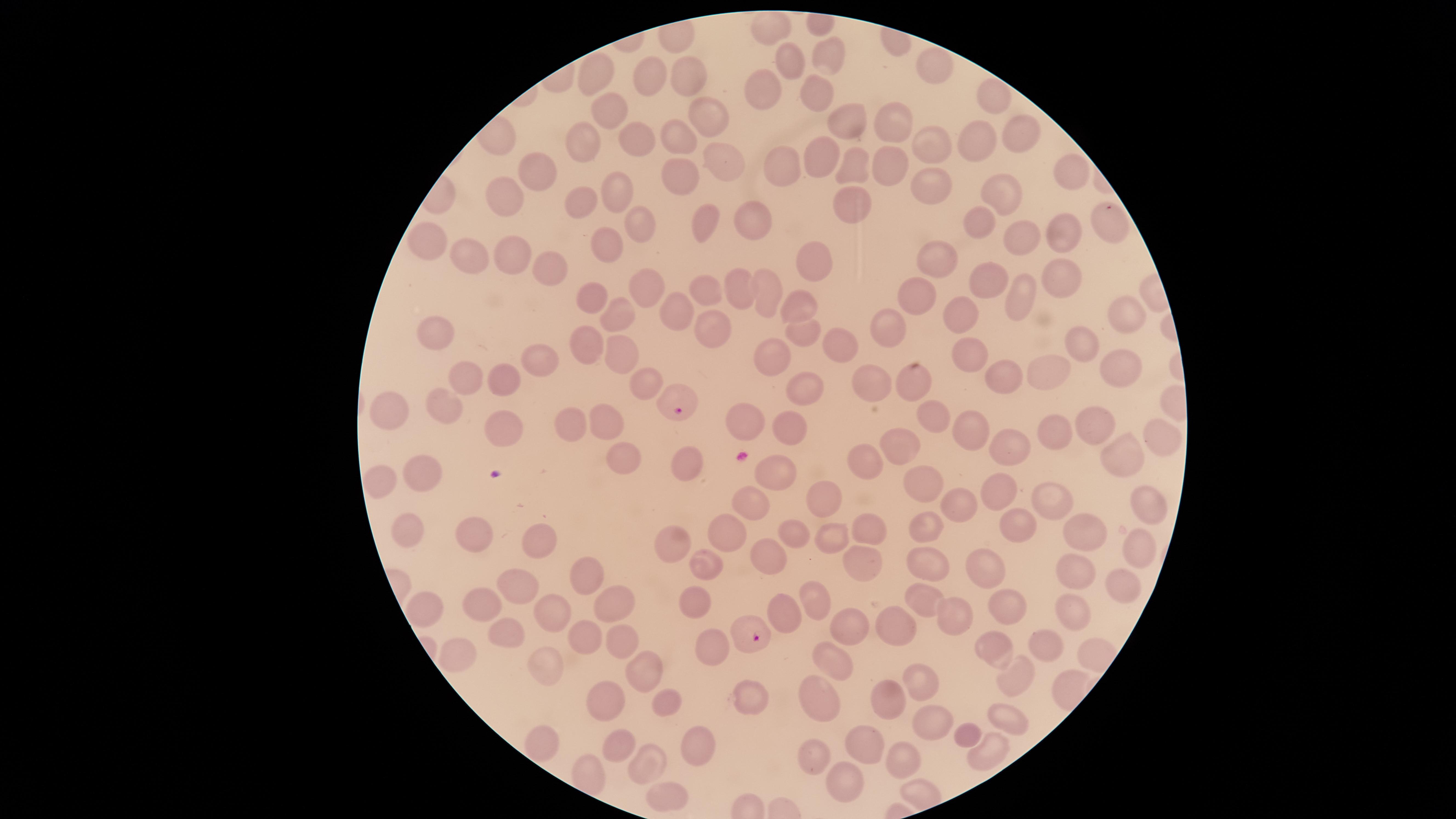
presence = malaria parasites seen
species = Plasmodium falciparum
parasitized RBCs = approximate marker points as [x, y] in pixels: [677, 403], [752, 635]
stain = Giemsa
uninfected RBCs = approximate marker points as [x, y] in pixels: [771, 21], [826, 53], [797, 61], [933, 67], [648, 75], [687, 76], [595, 80], [761, 85], [816, 93], [994, 96], [613, 108], [708, 118], [849, 120], [896, 121], [1023, 134], [638, 135], [975, 140], [588, 141], [680, 142], [931, 149], [812, 156], [782, 162], [884, 162], [722, 164], [850, 164], [1068, 167], [540, 170], [680, 176], [939, 184], [614, 186], [1001, 195], [507, 198], [582, 202], [850, 207], [752, 215], [1106, 218], [636, 224], [703, 224], [976, 226], [1061, 233], [1022, 237], [430, 243], [611, 244], [473, 251], [515, 256], [937, 256], [807, 260], [553, 270], [1059, 277], [989, 278], [740, 284], [647, 290], [762, 290], [707, 291], [592, 296], [920, 298], [1018, 298], [794, 305], [1128, 310], [677, 312], [956, 315], [614, 318], [893, 324], [711, 330], [441, 334], [806, 338], [586, 340], [1081, 342], [838, 344], [622, 355], [771, 358], [970, 358], [1125, 360], [544, 361], [1043, 373], [1001, 377], [506, 379], [871, 379], [473, 383], [645, 383], [912, 384], [801, 388], [393, 411], [450, 411], [741, 418], [929, 420], [1093, 423], [611, 425], [498, 428], [575, 428], [790, 428], [1048, 431], [969, 432], [1156, 442], [1004, 450], [901, 451], [624, 459], [1121, 459], [867, 463], [684, 466], [775, 471], [421, 477], [376, 480], [926, 480], [1002, 488], [824, 494], [752, 502], [961, 505], [1046, 505], [1146, 505], [868, 525], [925, 526], [1018, 526], [402, 529], [785, 531], [728, 533], [475, 534], [1079, 536], [830, 538], [679, 542], [542, 545], [1139, 551], [772, 557], [860, 562], [712, 563], [925, 563], [583, 570], [989, 573], [1073, 574], [1121, 581], [522, 588], [921, 599], [482, 600], [616, 600], [817, 600], [699, 603], [783, 608], [556, 610], [1008, 611], [1063, 613], [953, 615], [434, 616], [846, 628], [895, 628], [509, 631], [582, 637], [621, 638], [1050, 644], [709, 648], [996, 651], [457, 654], [830, 664], [547, 665], [646, 670], [1019, 678], [926, 688], [603, 699], [816, 701], [664, 702], [749, 704], [887, 704], [1001, 718], [926, 726], [967, 735], [621, 744], [866, 744], [700, 745], [544, 746], [990, 754], [813, 758], [643, 762], [905, 769], [846, 783], [664, 800]
capture = smartphone photograph through the microscope eyepiece
field of view = single
preparation = thin blood film
visible region = circular
image size = 1456×819 pixels